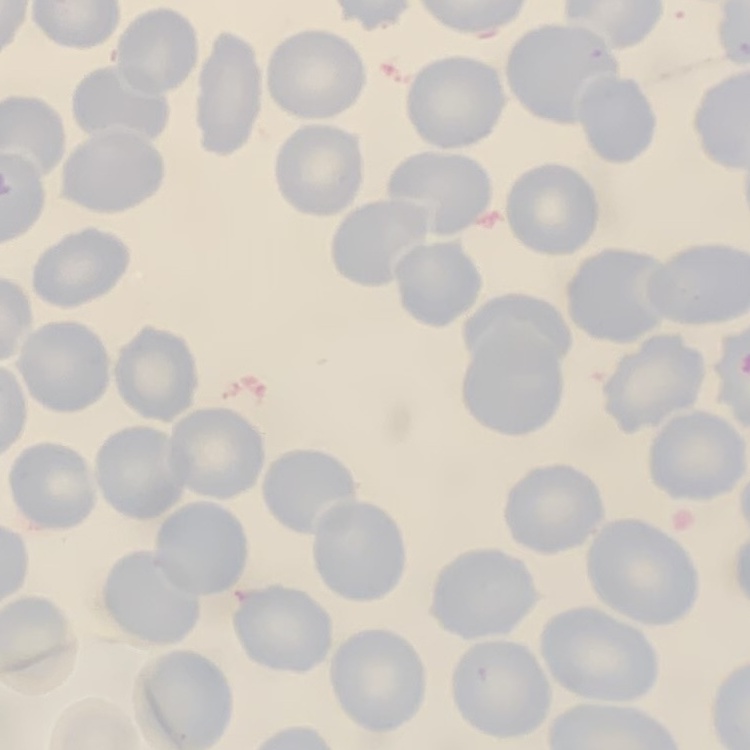
Summary:
  - Erythrocyte morphology: no rouleaux formation
  - Preparation: thin peripheral smear
  - Stain: Field's or Giemsa
  - Image type: one tile cut from a larger photomicrograph